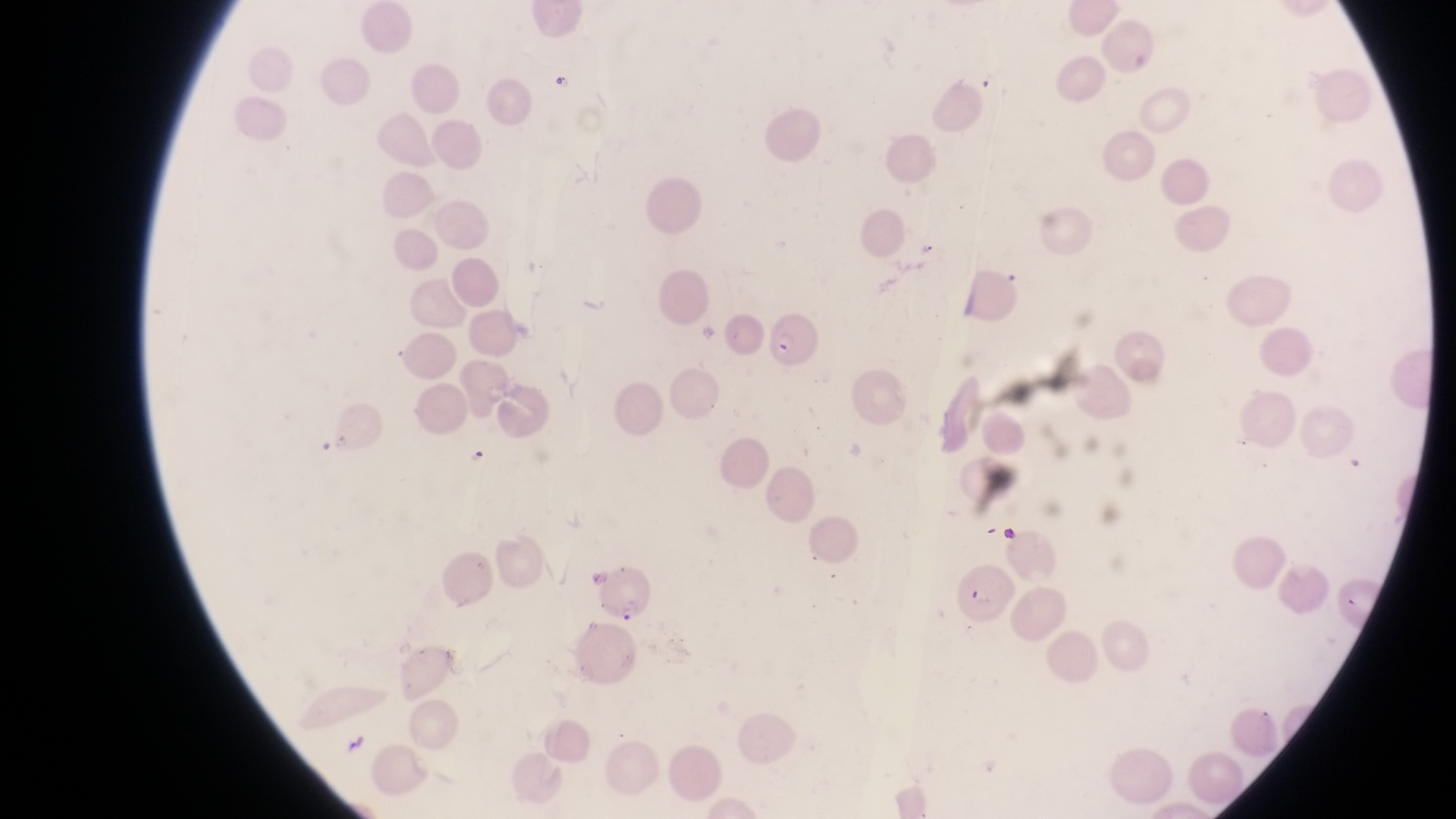 Approximate bounding boxes as {left, top, right, bottom} in pixels. Parasitised red blood cell locations: {766, 311, 816, 369}, {594, 563, 653, 623}. Artifact (platelet-like body, stain precipitate, or debris) locations: {548, 66, 572, 96}. Magnification of 1000x. Thin blood film. Photographed through the eyepiece of an Olympus CX-23 microscope with a smartphone camera. Sample from Uganda. Image is 1456×819 pixels. One field of view.